Classify this cell by malaria status.
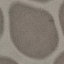

Uninfected.

{
  "stain": "Giemsa",
  "image_type": "cell patch, automatically extracted from a larger field of view and resized to 64 × 64 pixels",
  "preparation": "thin blood smear",
  "capture": "smartphone camera at the microscope eyepiece"
}